Locate every blood parasite and identify its species.
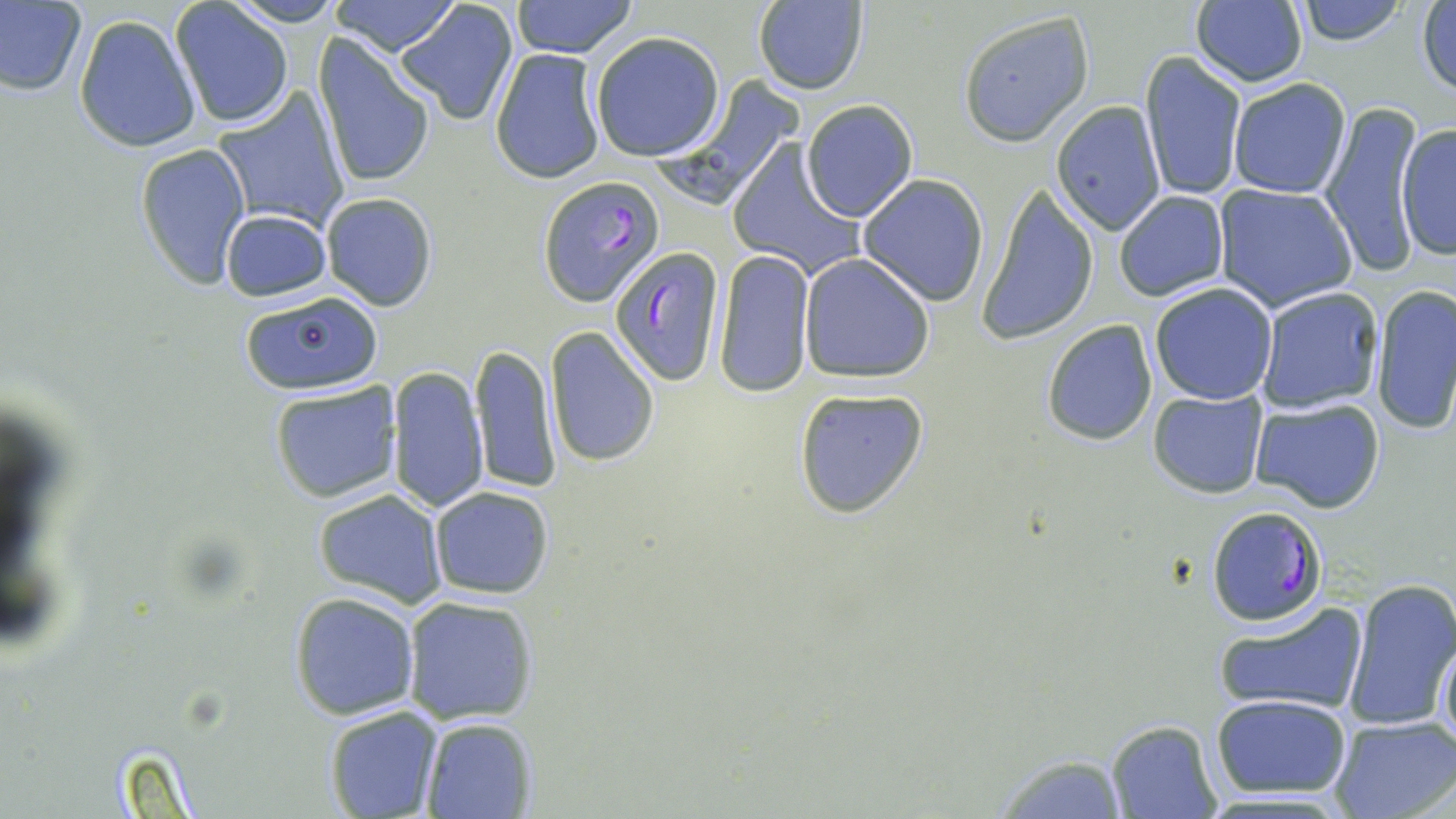
Approximate bounding boxes as [x1, y1, x2, y2] in pixels.
Plasmodium falciparum-infected red blood cells: [538, 175, 664, 307], [609, 245, 725, 386], [1205, 506, 1326, 628].
No Plasmodium ovale, Plasmodium malariae, Plasmodium vivax, Babesia divergens, or Trypanosoma brucei observed.

{
  "slide_level_diagnosis": "Plasmodium falciparum",
  "stain": "May-Grünwald-Giemsa",
  "modality": "light microscopy",
  "magnification": "1000x",
  "field_of_view": "single",
  "uninfected_red_blood_cell_locations": "approximate bounding boxes as [x1, y1, x2, y2] in pixels: [0, 0, 87, 98], [327, 0, 462, 56], [510, 0, 639, 59], [1292, 0, 1412, 48], [228, 1, 345, 27], [752, 1, 870, 95], [395, 2, 520, 127], [1189, 2, 1309, 87], [170, 3, 293, 128], [1417, 3, 1456, 97], [954, 10, 1096, 148], [73, 14, 201, 154], [590, 31, 726, 161], [313, 35, 436, 190], [488, 49, 608, 183], [1139, 50, 1248, 202], [1229, 77, 1352, 199], [211, 86, 349, 232], [801, 99, 916, 221], [1051, 101, 1166, 235], [1318, 101, 1423, 275], [1395, 121, 1456, 262], [135, 142, 251, 288], [725, 143, 863, 284], [857, 175, 990, 305], [978, 182, 1098, 345], [1213, 184, 1357, 312], [1114, 190, 1230, 302], [321, 192, 438, 311], [220, 209, 333, 302], [712, 248, 815, 397], [799, 253, 936, 382], [1149, 282, 1278, 405], [1370, 285, 1456, 436], [1254, 286, 1384, 415], [238, 290, 385, 396], [1041, 318, 1157, 445], [544, 326, 662, 471], [470, 344, 561, 494], [385, 364, 488, 514], [269, 379, 402, 503], [792, 387, 930, 519], [1147, 389, 1270, 497], [1250, 399, 1387, 514], [429, 486, 554, 599], [311, 489, 449, 609], [1340, 576, 1456, 733], [289, 590, 419, 720], [401, 594, 541, 724], [1211, 599, 1370, 717], [1436, 638, 1456, 754], [1210, 694, 1354, 801], [323, 706, 443, 818], [417, 715, 538, 818], [1328, 715, 1456, 819], [1103, 719, 1224, 819], [982, 754, 1131, 818]",
  "preparation": "thin blood smear",
  "image_size": "1456×819 pixels"
}